Name the parasite shown.
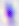
This is Toxoplasma gondii.

magnification = 400x
modality = micrograph